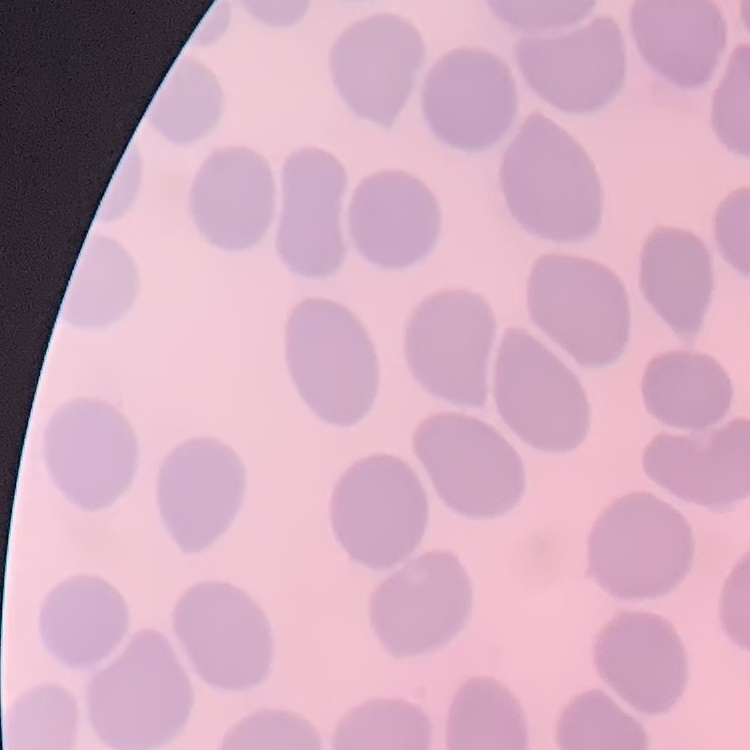
red blood cell morphology = no rouleaux formation
stain = Field's or Giemsa
preparation = thin blood smear
image type = one tile cut from a larger photomicrograph